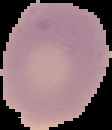
Summary:
  - Result: no Plasmodium parasites seen
  - Image type: segmented cell region with the area outside set to black
  - Preparation: thin blood film
  - Image size: 112×130 pixels